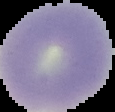

image size = 115×112 pixels
preparation = thin blood smear
result = no malaria parasites detected
image type = cell region segmented out of the field of view; surrounding area masked to black